Locate every Plasmodium parasite.
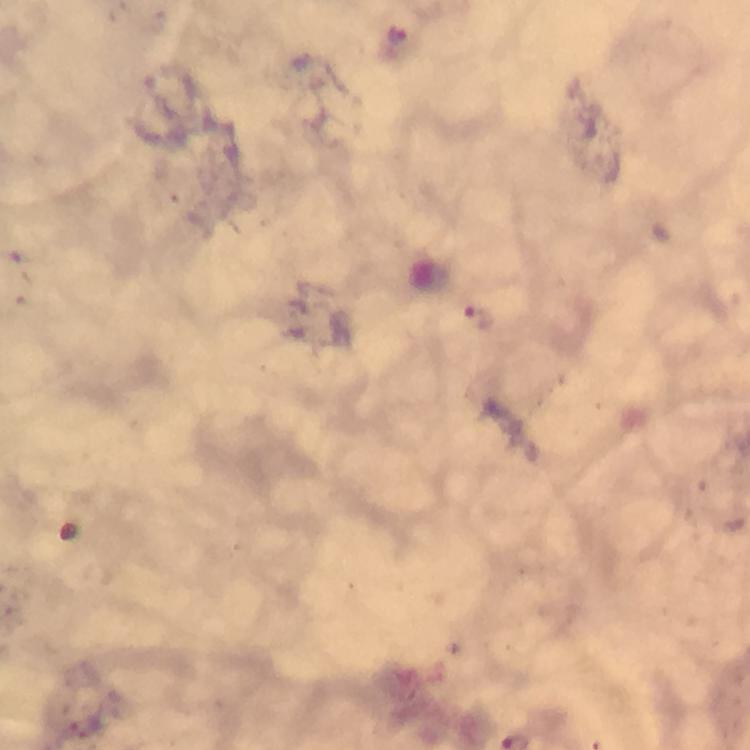

Approximate object centers, in pixels from the top-left corner.
Plasmodium parasites: (x=393, y=34), (x=481, y=320).

magnification: 100x
cropped_from: a single field of view
immersion_oil: used
capture: smartphone photograph through a microscope
preparation: thick blood film
stain: Giemsa
context: from a malaria diagnostic workup
image_size: 750×750 pixels